Assess this cell for malaria.
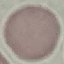
Uninfected.

Cell patch, automatically extracted from a larger field of view and resized to 64 × 64 pixels. Giemsa stain. Thin smear of blood. Acquired by smartphone through the microscope eyepiece.